Report the malaria status.
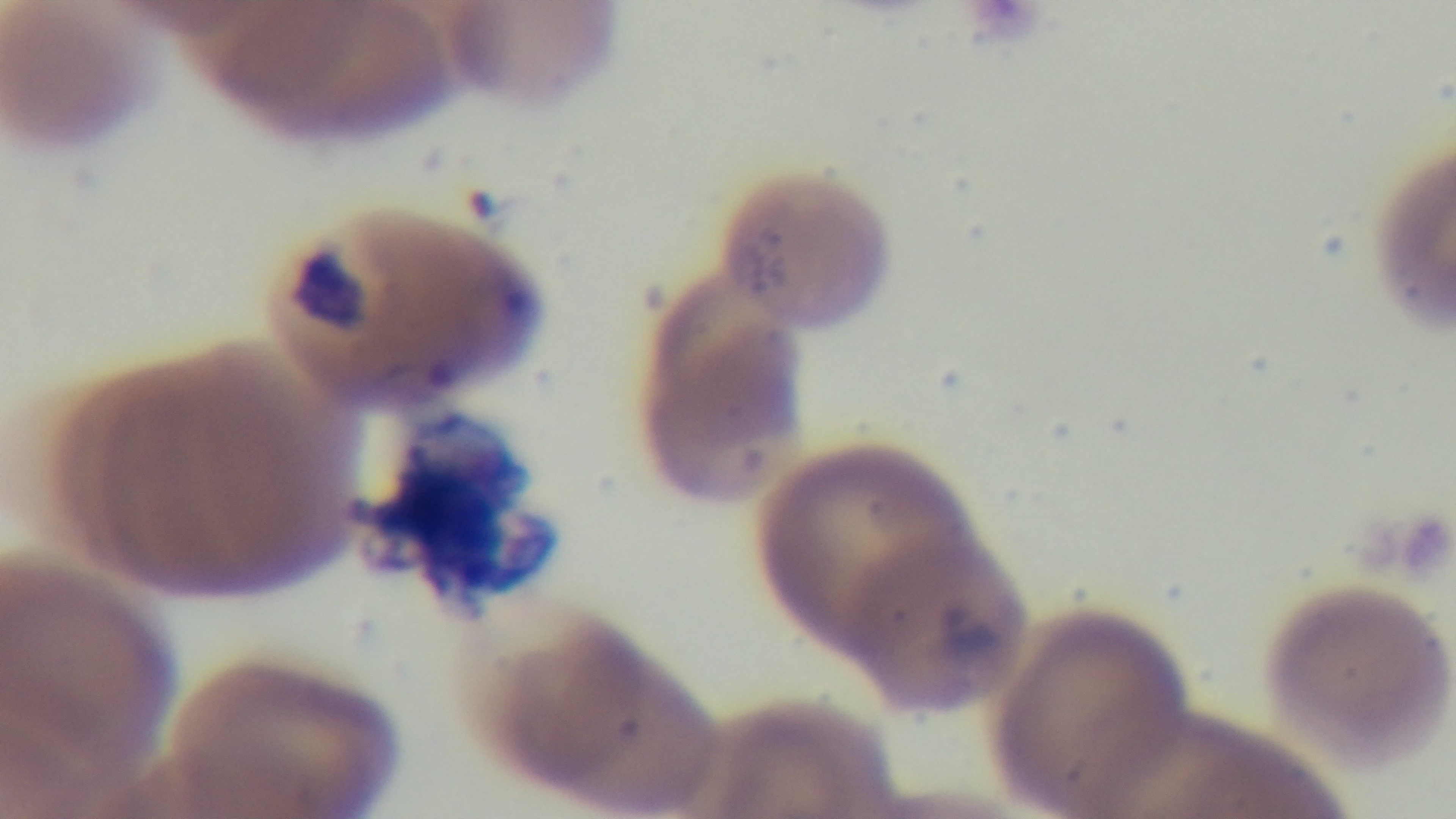
Positive.

Mounted 4K digital camera. Preparation: thin. Photomicrograph. Giemsa stain. One field from the slide. Oil-immersion objective, 100x.